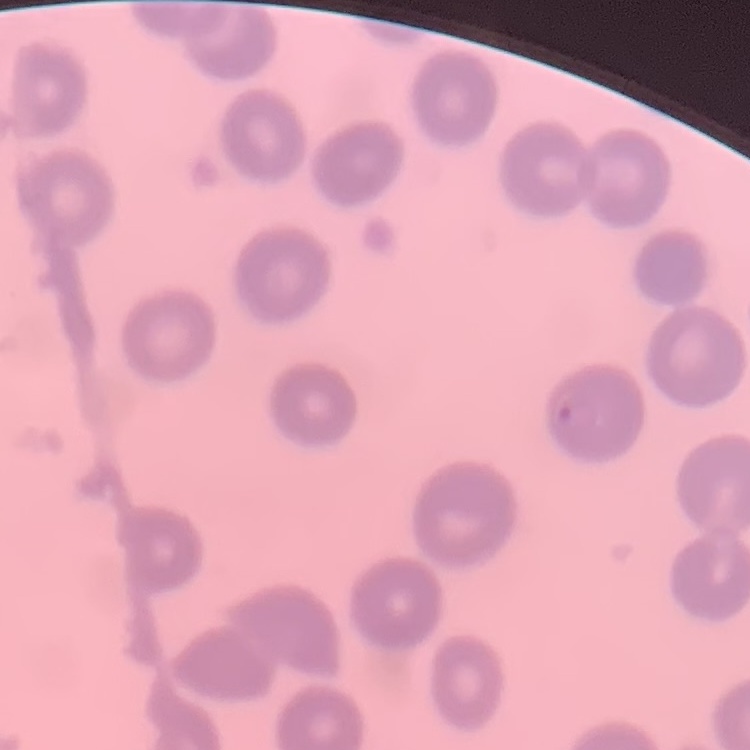
The red blood cells show no rouleaux formation. Thin blood smear. Square crop of a larger photomicrograph. Field's or Giemsa stain.